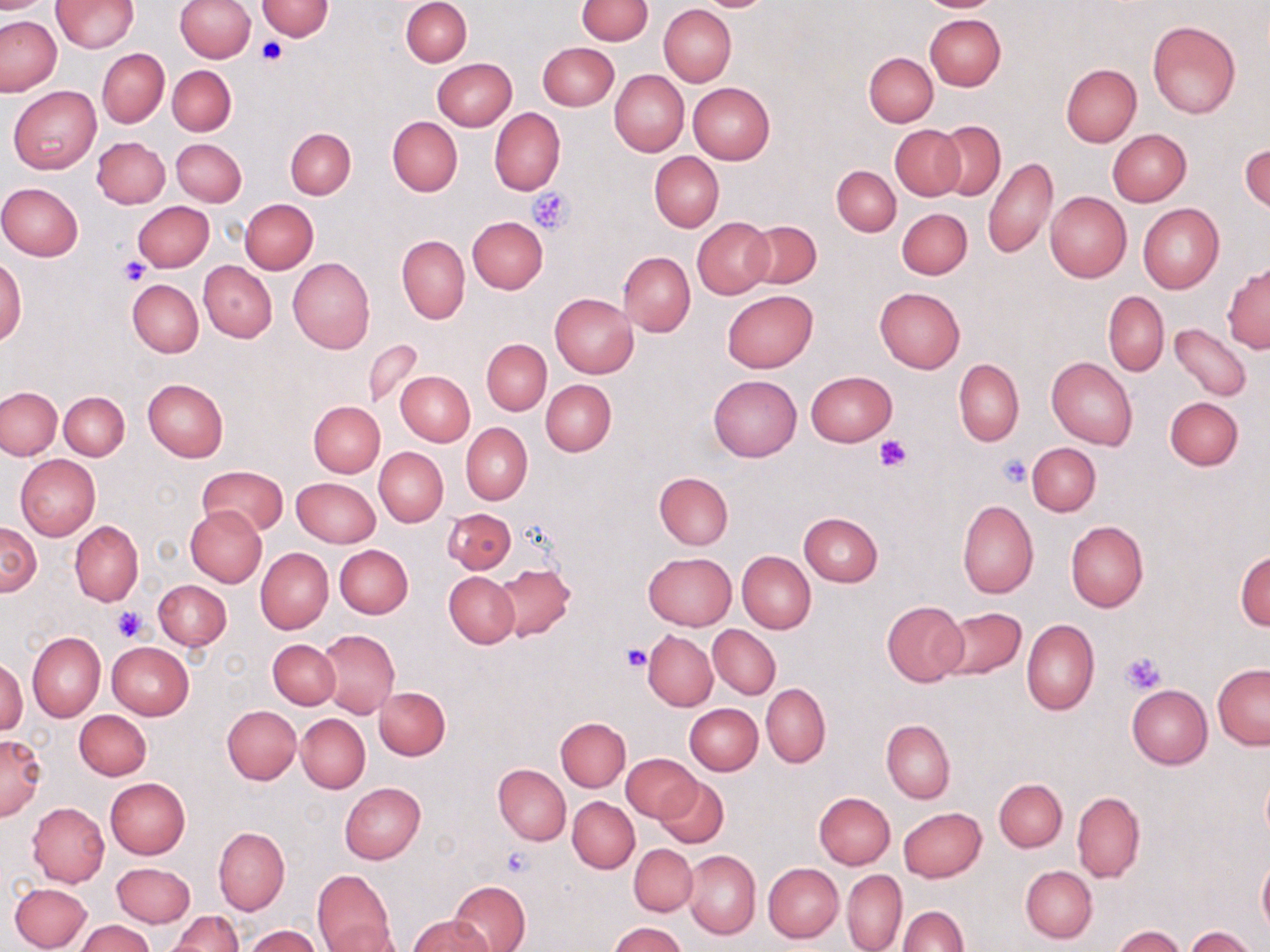
Summary:
  - Coordinate format: approximate bounding boxes as (x1, y1, x2, y2) in pixels
  - Uninfected red blood cell locations: (0, 0, 56, 14), (175, 0, 256, 62), (401, 0, 471, 67), (576, 0, 653, 46), (916, 0, 1005, 12), (51, 1, 139, 52), (257, 1, 334, 40), (701, 1, 770, 11), (659, 5, 736, 85), (925, 14, 1005, 90), (0, 15, 63, 97), (1147, 20, 1242, 118), (538, 42, 618, 110), (97, 48, 169, 128), (864, 52, 937, 126), (433, 58, 516, 130), (1060, 63, 1141, 147), (168, 65, 236, 136), (610, 70, 688, 156), (688, 83, 775, 164), (9, 86, 101, 174), (490, 108, 565, 195), (387, 117, 461, 195), (934, 121, 1004, 200), (891, 125, 964, 200), (286, 128, 356, 199), (1106, 129, 1190, 206), (92, 137, 169, 208), (172, 138, 246, 206), (1241, 144, 1268, 213), (650, 152, 723, 230), (984, 157, 1057, 259), (831, 165, 900, 236), (0, 183, 84, 260), (1045, 191, 1131, 283), (241, 199, 318, 273), (133, 201, 214, 271), (1137, 203, 1224, 294), (897, 208, 972, 280), (467, 216, 547, 294), (693, 217, 774, 298), (746, 220, 821, 289), (397, 236, 470, 323), (618, 251, 695, 336), (1, 255, 27, 345), (287, 257, 374, 353), (199, 260, 277, 342), (1223, 264, 1269, 353), (127, 279, 203, 357), (875, 287, 965, 372), (722, 291, 817, 372), (1104, 291, 1169, 376), (549, 294, 638, 379), (1170, 323, 1251, 402), (362, 339, 424, 411), (482, 339, 551, 415), (1047, 357, 1137, 450), (954, 360, 1023, 445), (806, 370, 897, 446), (396, 371, 475, 445), (708, 375, 802, 461), (143, 378, 228, 461), (541, 379, 616, 457), (1, 387, 62, 460), (59, 392, 130, 459), (1165, 397, 1243, 470), (308, 401, 384, 476), (461, 423, 532, 505), (1028, 443, 1100, 516), (374, 447, 447, 526), (16, 455, 100, 539), (199, 465, 286, 535), (654, 472, 733, 550), (292, 477, 380, 548), (956, 499, 1037, 598), (185, 504, 266, 588), (446, 508, 519, 576), (799, 512, 883, 587), (70, 521, 143, 605), (1066, 521, 1148, 612), (0, 523, 40, 597), (335, 545, 413, 619), (256, 548, 333, 633), (737, 551, 815, 633), (1235, 551, 1270, 631), (642, 552, 736, 630), (493, 564, 575, 641), (444, 571, 519, 647), (154, 580, 231, 650), (881, 601, 968, 686), (937, 606, 1027, 682), (1021, 619, 1099, 715), (708, 626, 780, 698), (315, 628, 400, 719), (27, 631, 105, 722), (644, 631, 717, 711), (268, 639, 340, 709), (107, 642, 193, 719), (0, 658, 27, 736), (1212, 664, 1269, 749), (761, 684, 830, 767), (1127, 685, 1212, 768), (374, 686, 450, 760), (685, 703, 763, 775), (222, 704, 301, 785), (75, 709, 152, 780), (297, 714, 370, 792), (555, 717, 631, 792), (881, 719, 955, 803), (0, 735, 46, 819), (622, 753, 701, 823), (494, 764, 571, 844), (104, 777, 191, 859), (655, 777, 728, 848), (994, 779, 1067, 851), (340, 782, 425, 863), (814, 791, 895, 869), (1071, 791, 1145, 882), (568, 797, 639, 872), (28, 803, 109, 886), (898, 807, 986, 881), (213, 827, 289, 914), (629, 844, 698, 916), (684, 850, 760, 939), (1257, 856, 1270, 936), (763, 862, 844, 943), (111, 863, 195, 928), (1020, 864, 1097, 943), (311, 869, 396, 950), (841, 870, 909, 952), (448, 880, 531, 952), (8, 882, 92, 951), (898, 906, 967, 952), (166, 911, 242, 952), (409, 914, 489, 952), (76, 920, 155, 952), (609, 922, 687, 952), (320, 923, 404, 951), (244, 925, 323, 952), (1113, 926, 1184, 952), (1185, 926, 1256, 952)
  - Platelet locations: (257, 37, 288, 65), (527, 188, 575, 235), (119, 258, 152, 286), (875, 437, 911, 471), (997, 453, 1032, 488), (111, 605, 150, 644), (620, 644, 653, 672), (1121, 650, 1167, 694), (500, 846, 537, 878)
  - Slide-level diagnosis: no evidence of blood parasites
  - Magnification: 1000x
  - Preparation: thin blood smear
  - Modality: optical microscopy
  - Image size: 1270×952 pixels
  - Field of view: single
  - Stain: May-Grünwald-Giemsa